Assess for malaria.
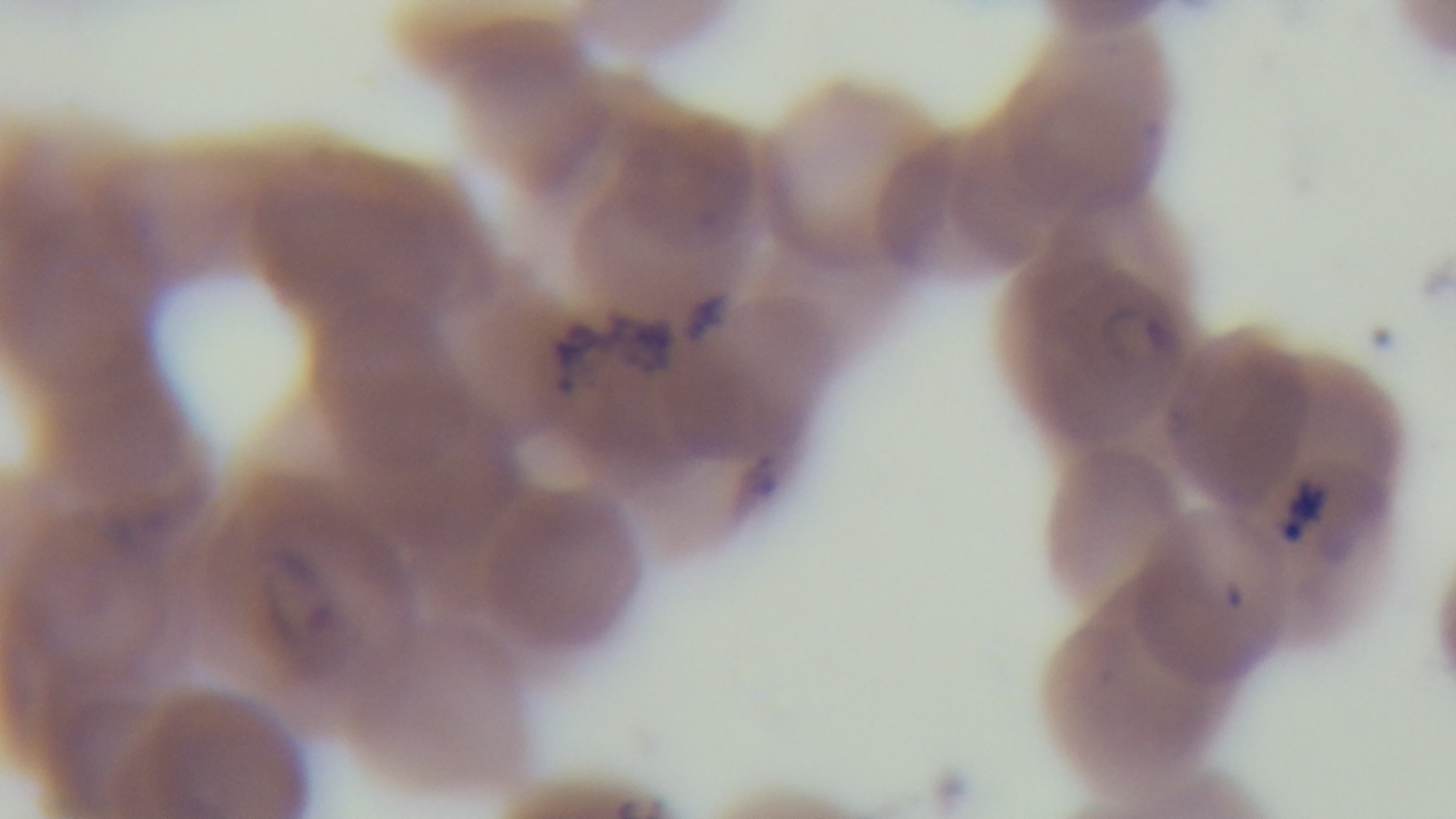

Positive.

Single field of view. Preparation: thin blood film. Giemsa-stained. Photomicrograph. Captured with a mounted 4K digital camera. Oil-immersion objective, 100x.